Describe the morphology of the red blood cells.
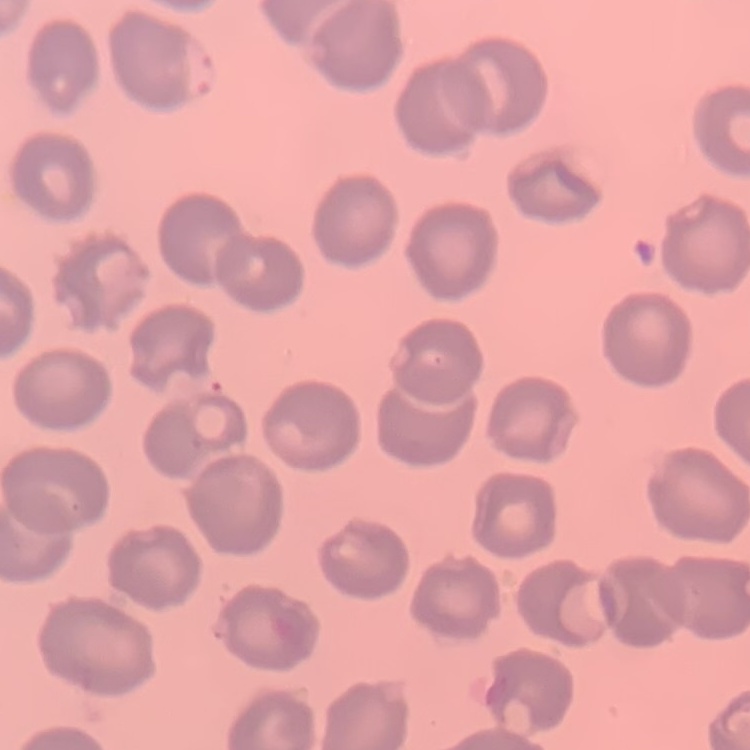
They show no rouleaux formation.

Thin blood film. Square crop of a larger photomicrograph. Field's or Giemsa stain.